Assess the morphology of the erythrocytes.
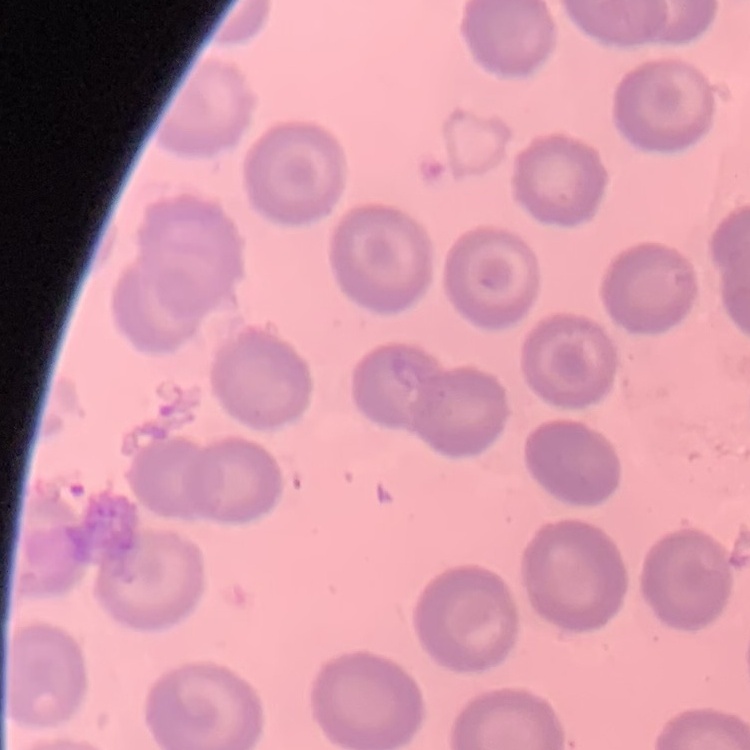

No rouleaux formation.

stain = Field's or Giemsa
image type = square crop of a larger photomicrograph
preparation = thin peripheral smear